Identify the parasite.
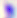

This is Toxoplasma gondii.

Photomicrograph. Captured at 400x magnification.